Classify this cell by malaria status.
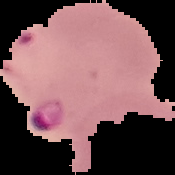

It is parasitized.

The area outside the segmented cell region is set to black. From a thin blood film. Image is 175×175 pixels.